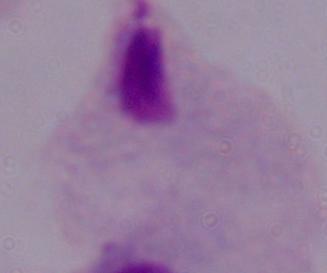

Photomicrograph. A trichomonad is seen. 1000x magnification.